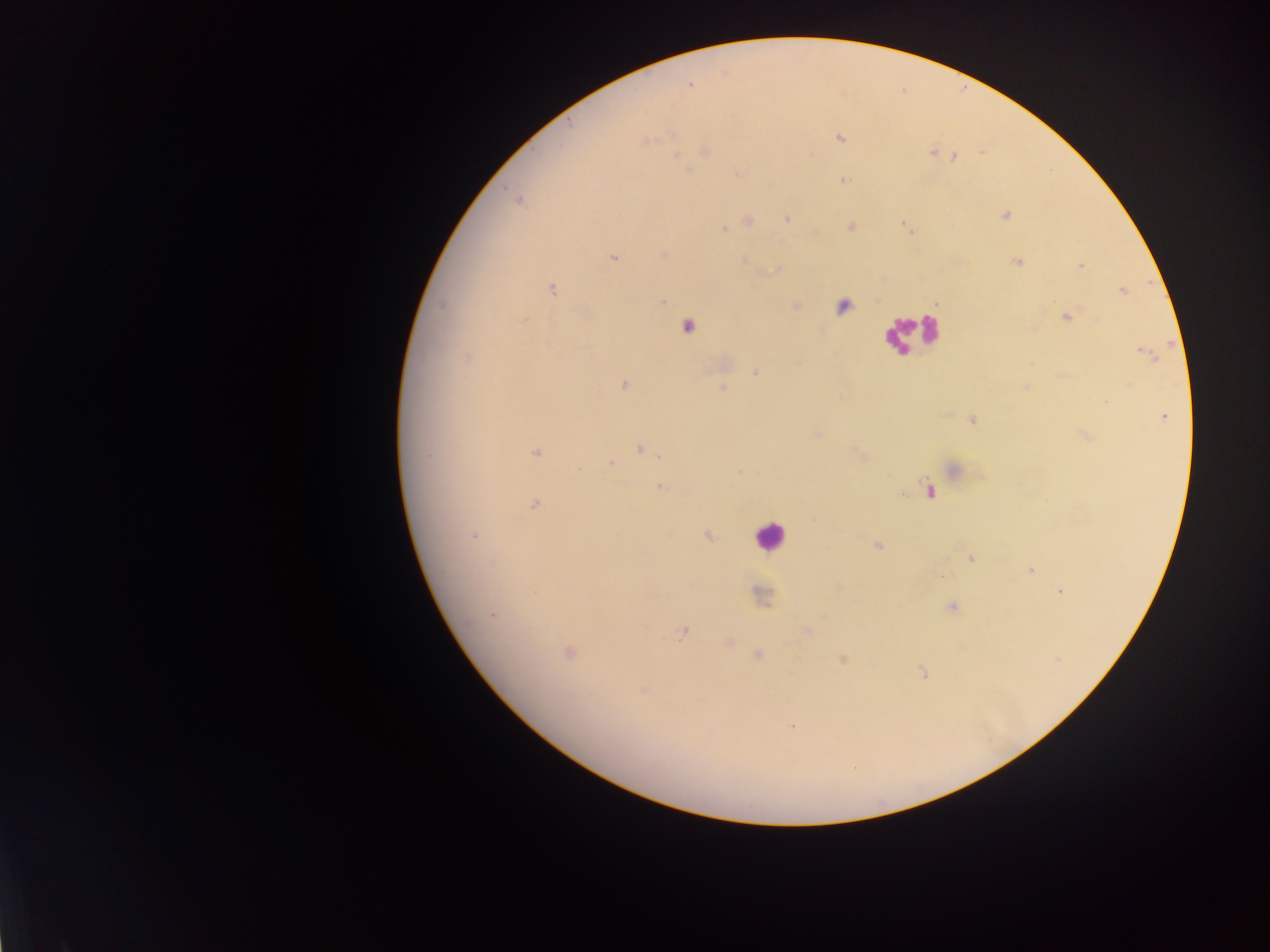 Approximate centers as {x, y} in pixels. Malaria parasite locations: {839, 138}, {931, 153}, {954, 157}, {845, 180}, {506, 189}, {1005, 215}, {786, 217}, {748, 219}, {850, 227}, {724, 228}, {661, 253}, {612, 258}, {1017, 261}, {1081, 266}, {551, 288}, {1120, 291}, {663, 299}, {441, 304}, {1067, 317}, {524, 321}, {1142, 352}, {467, 357}, {755, 372}, {623, 385}, {721, 387}, {973, 419}, {535, 452}, {859, 453}, {661, 457}, {609, 464}, {739, 470}, {579, 471}, {924, 479}, {659, 486}, {900, 494}, {534, 503}, {474, 534}, {707, 534}, {877, 545}, {972, 559}, {1029, 569}, {1059, 591}, {953, 608}, {493, 614}, {681, 632}, {924, 674}, {790, 726}. Leukocyte locations: {906, 331}, {770, 539}. Mobile-phone photograph taken through the microscope. Thick blood smear. Sample from Ghana. Single field of view. Image is 1270×952 pixels.